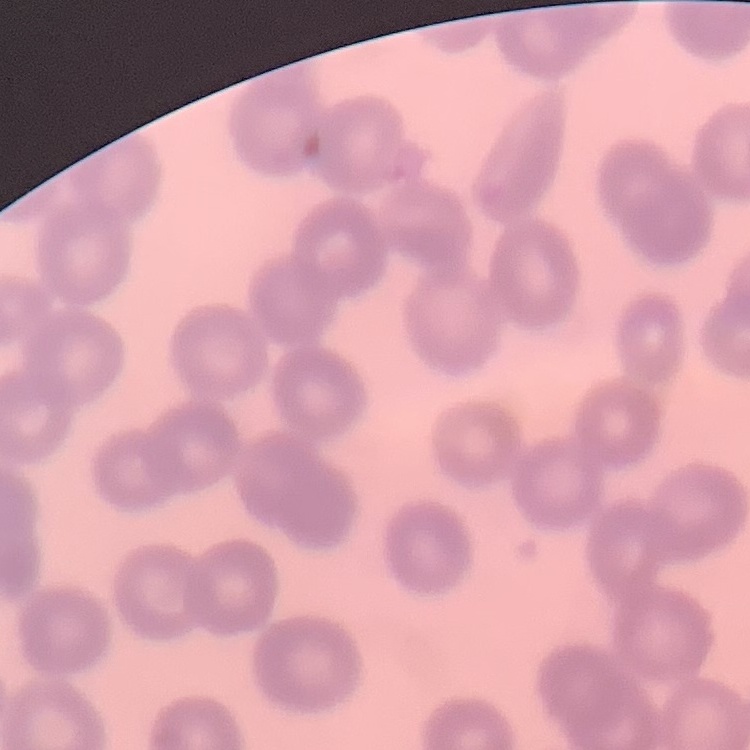
Summary:
  - Erythrocyte morphology: no rouleaux formation
  - Image type: one tile cut from a larger photomicrograph
  - Preparation: thin blood smear
  - Stain: Field's or Giemsa